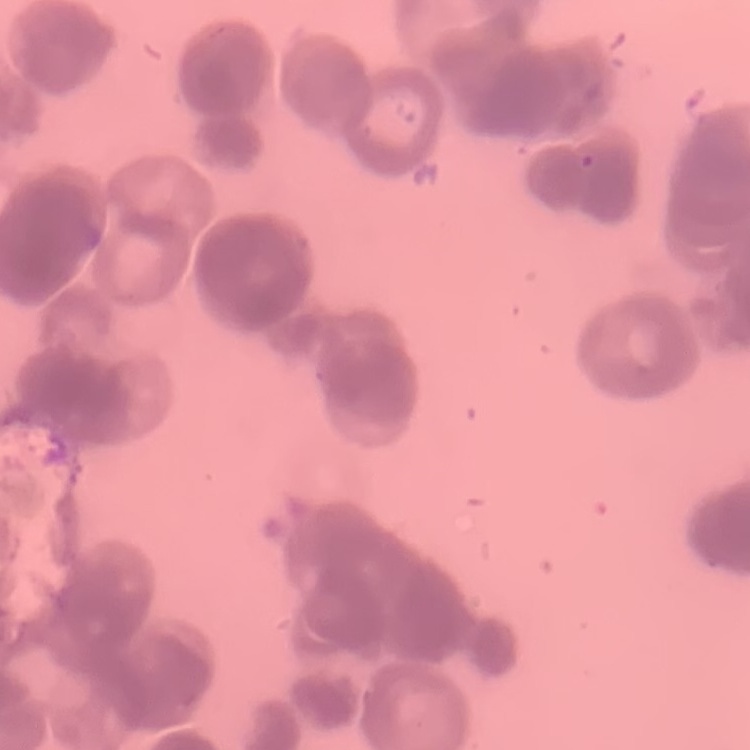
red blood cell morphology = rouleaux formation
stain = Field's or Giemsa
image type = one tile cut from a larger photomicrograph
preparation = thin blood film